Name the parasite shown.
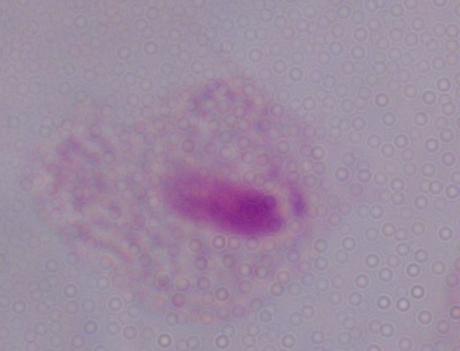

A trichomonad.

Summary:
  - Magnification: 1000x
  - Modality: photomicrograph